Classify this cell by malaria status.
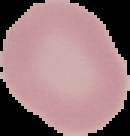

It is uninfected.

image size = 130×136 pixels
image type = segmented cell region on a black background
preparation = thin blood smear